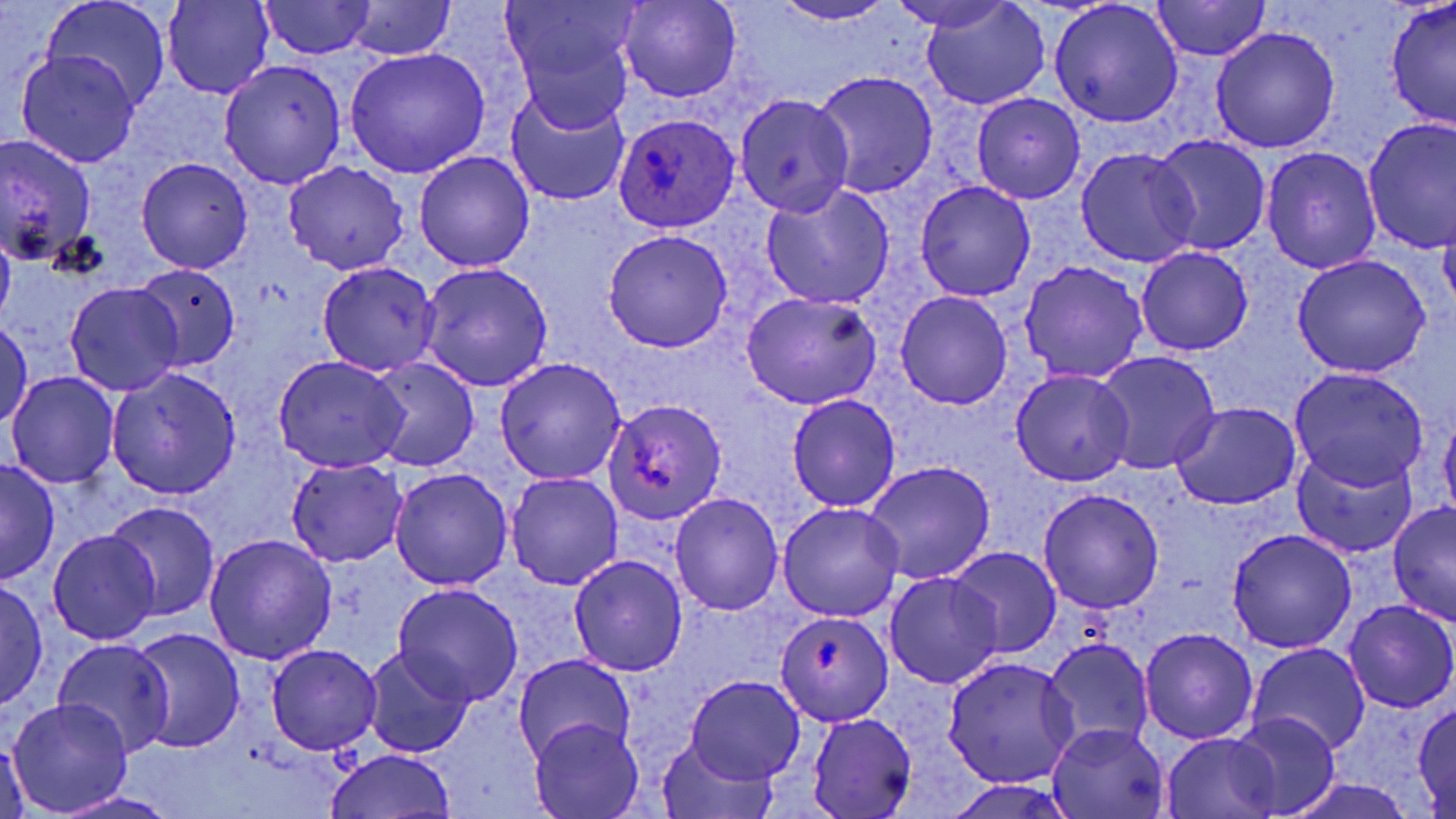

Approximate bounding boxes as (x1,y1)-(x2,y2) corner pairs in pixels. Uninfected red blood cell locations: (41,0)-(170,111), (256,0)-(380,59), (617,0)-(741,102), (886,0)-(1021,35), (920,0)-(1049,109), (1149,0)-(1272,63), (1384,0)-(1456,130), (162,1)-(274,100), (336,1)-(457,60), (771,1)-(901,26), (498,2)-(643,121), (1050,2)-(1184,127), (1211,27)-(1340,151), (343,48)-(490,178), (16,53)-(142,167), (219,59)-(346,189), (812,70)-(939,198), (506,87)-(632,207), (971,92)-(1085,204), (734,94)-(854,216), (1363,119)-(1456,252), (0,134)-(99,265), (1151,136)-(1270,255), (1262,147)-(1382,274), (1075,148)-(1200,268), (415,152)-(534,272), (136,158)-(253,274), (282,161)-(409,275), (915,181)-(1036,300), (760,184)-(895,311), (0,223)-(15,335), (602,230)-(732,353), (1136,247)-(1253,355), (1291,254)-(1431,378), (316,261)-(442,377), (1020,261)-(1148,383), (418,262)-(554,392), (134,265)-(241,371), (65,283)-(184,395), (741,291)-(882,410), (896,291)-(1013,409), (1,320)-(32,431), (1093,352)-(1221,476), (271,355)-(409,473), (365,356)-(480,473), (493,357)-(627,485), (106,366)-(241,498), (1011,369)-(1135,487), (1288,369)-(1428,491), (7,373)-(120,488), (786,394)-(901,512), (605,398)-(727,525), (1171,402)-(1299,510), (1440,406)-(1456,526), (1293,444)-(1418,557), (0,458)-(59,585), (285,458)-(408,567), (864,461)-(995,584), (391,467)-(513,590), (506,471)-(624,591), (1037,488)-(1165,613), (670,492)-(784,616), (104,501)-(219,620), (1387,501)-(1456,628), (777,502)-(905,621), (1227,529)-(1357,653), (49,530)-(160,646), (205,533)-(338,666), (947,546)-(1061,659), (569,555)-(688,676), (883,571)-(1005,689), (0,579)-(48,708), (393,582)-(525,707), (1343,600)-(1455,713), (775,610)-(894,725), (129,627)-(244,754), (1140,627)-(1259,745), (51,638)-(175,758), (1042,639)-(1154,756), (265,644)-(382,756), (1247,644)-(1371,757), (362,646)-(474,757), (513,654)-(636,766), (942,656)-(1079,788), (685,676)-(803,785), (8,699)-(132,814), (1413,702)-(1456,813), (808,713)-(917,818), (1229,713)-(1338,818), (530,719)-(645,819), (1047,723)-(1170,818), (0,732)-(32,819), (1164,733)-(1279,817), (655,737)-(777,817), (325,748)-(458,819), (1285,777)-(1421,819), (55,791)-(181,818). Plasmodium ovale-infected red blood cell locations: (614,111)-(741,231). Slide-level diagnosis: Plasmodium ovale. Image is 1456×819 pixels. Light microscopy. May-Grünwald-Giemsa-stained preparation. Thin blood film. Single field of view. Captured at 1000x magnification.